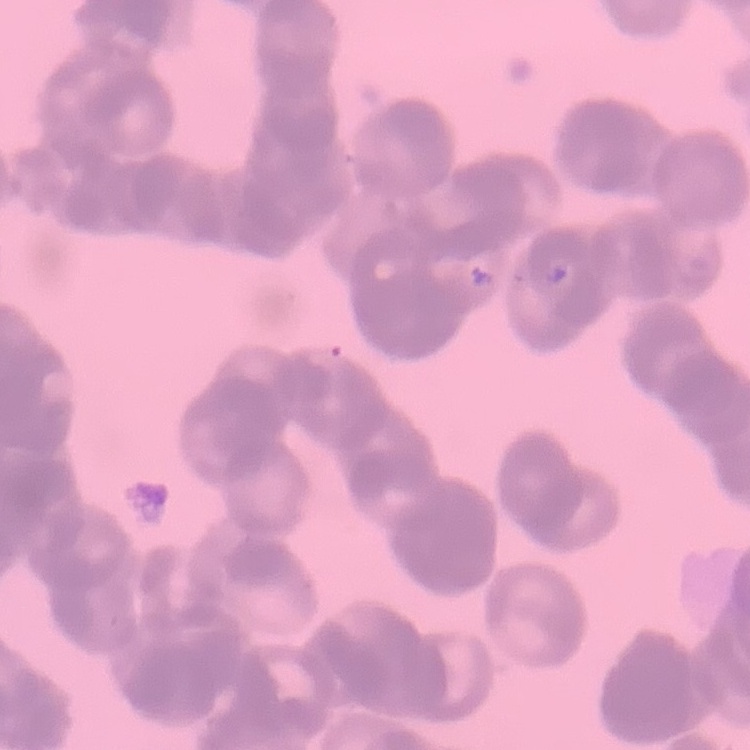
The erythrocytes exhibit rouleaux formation. Field's or Giemsa stain. One tile cut from a larger photomicrograph. Thin blood film.